Assess the morphology of the red blood cells.
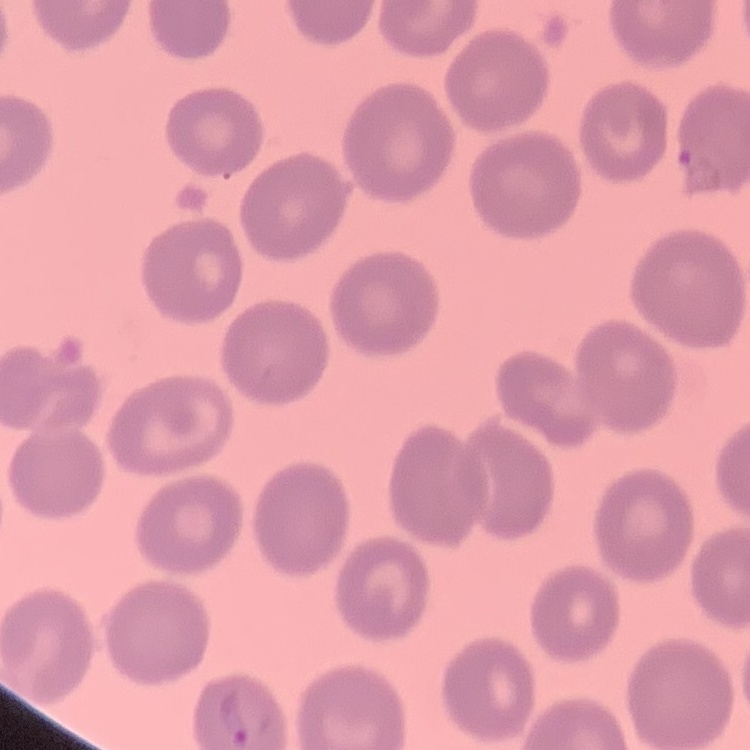

No rouleaux formation.

Square crop of a larger photomicrograph. Thin blood smear. Stained with either Field's or Giemsa.